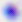

Summary:
  - Identification: Toxoplasma gondii
  - Magnification: 400x
  - Modality: photomicrograph